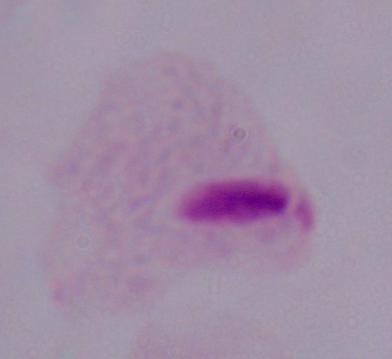

identification = trichomonad
magnification = 1000x
modality = micrograph